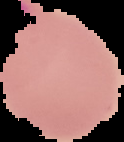 From a thin blood film. Image is 124×142 pixels. Result: malaria parasites detected. Cell region segmented out of the field of view; the surrounding area is masked to black.